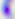
Summary:
  - Modality: photomicrograph
  - Identification: Toxoplasma gondii
  - Magnification: 400x